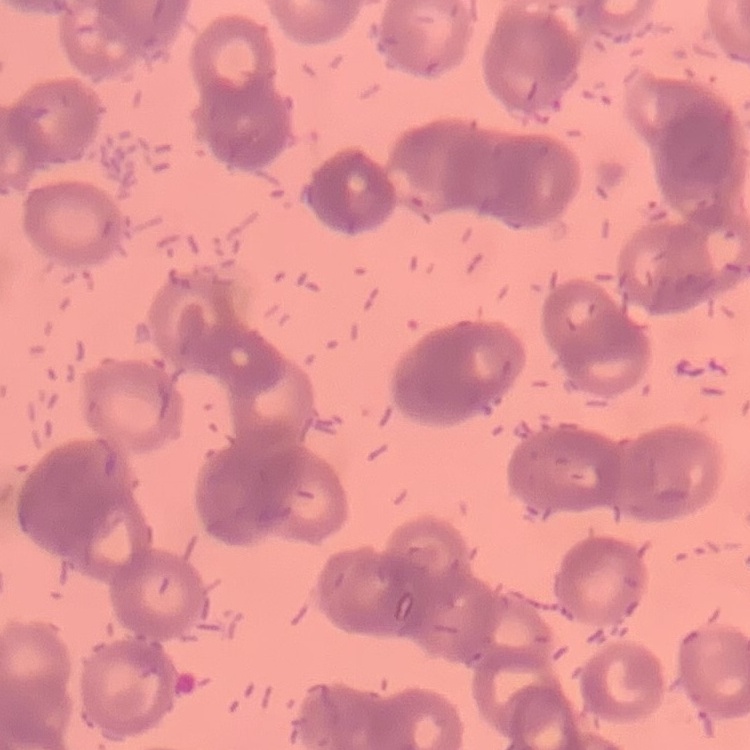

Summary:
  - Erythrocyte morphology: rouleaux formation
  - Preparation: thin peripheral smear
  - Image type: one tile cut from a larger photomicrograph
  - Stain: Field's or Giemsa